Identify the cell.
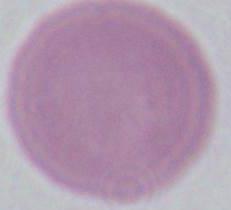

An erythrocyte.

Summary:
  - Magnification: 1000x
  - Modality: micrograph